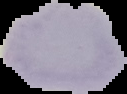 Result: negative for Plasmodium parasites. Image is 127×94 pixels. Segmented cell region on a black background. From a thin blood smear.